Assess this cell for malaria.
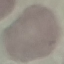

It is uninfected.

image_type: cell patch, automatically extracted from a larger field of view and resized to 64 × 64 pixels
preparation: thin blood smear
stain: Giemsa
capture: smartphone camera at the microscope eyepiece